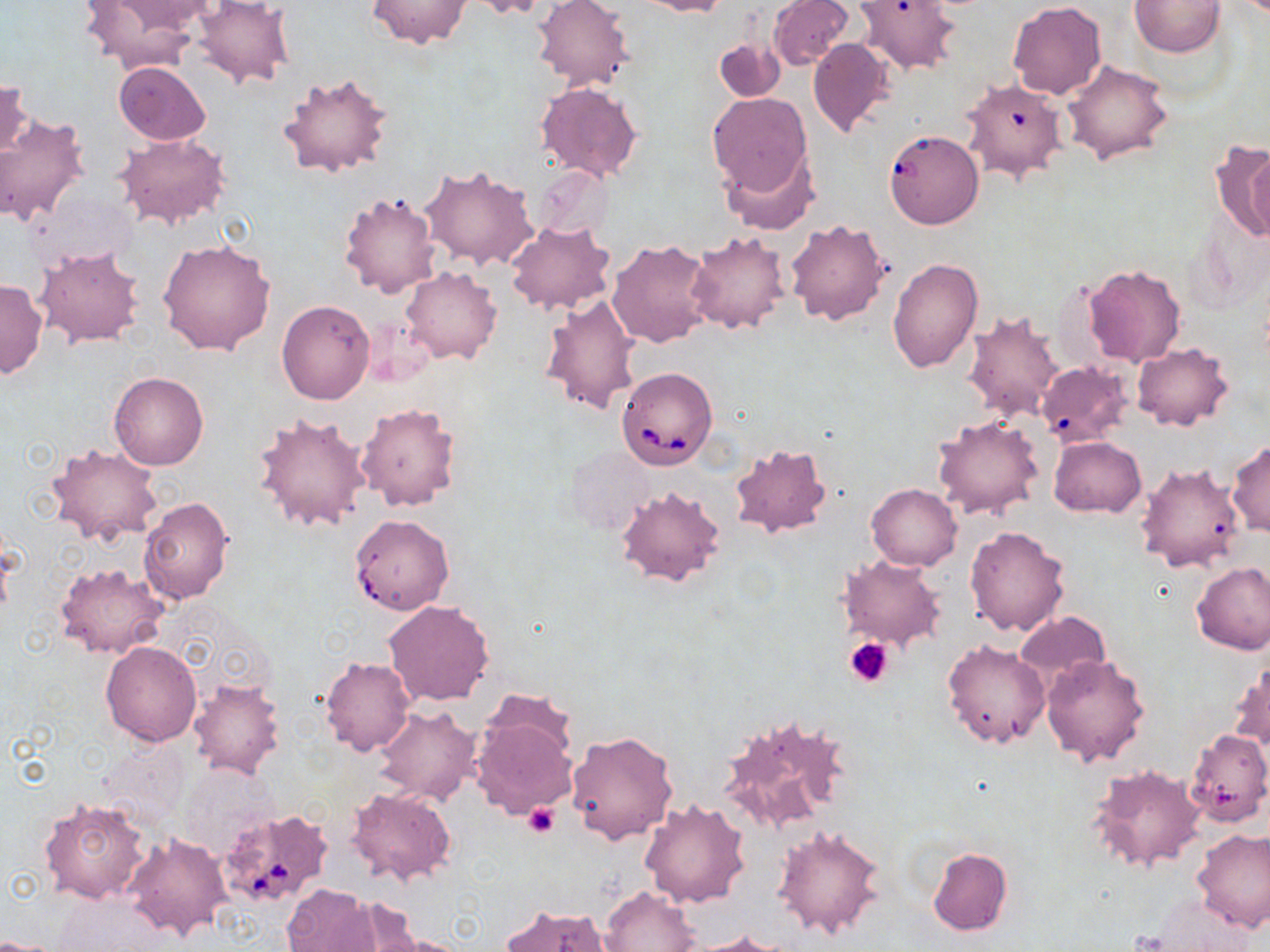 Approximate bounding boxes as (x1,y1)-(x2,y2) corner pairs in pixels. Platelet locations: (843,636)-(894,687), (524,802)-(559,839). Uninfected red blood cell locations: (365,0)-(474,49), (468,0)-(549,20), (531,0)-(633,91), (640,0)-(731,17), (767,0)-(853,71), (855,0)-(960,75), (1130,0)-(1225,57), (77,1)-(199,71), (105,1)-(217,36), (190,1)-(296,88), (1008,2)-(1107,99), (714,36)-(784,102), (807,38)-(895,138), (1063,60)-(1172,166), (112,62)-(212,145), (278,72)-(394,179), (1,76)-(33,168), (959,78)-(1067,185), (534,82)-(644,182), (707,93)-(812,195), (0,113)-(89,226), (887,130)-(986,234), (116,135)-(231,231), (1212,141)-(1270,240), (722,149)-(819,234), (420,165)-(538,272), (533,165)-(613,241), (339,192)-(441,299), (784,219)-(889,326), (506,220)-(616,314), (684,230)-(792,334), (156,238)-(276,355), (607,240)-(716,349), (33,244)-(146,349), (887,259)-(982,373), (1084,264)-(1186,366), (401,266)-(503,364), (0,279)-(46,378), (540,293)-(643,416), (277,300)-(376,405), (963,309)-(1065,422), (1131,341)-(1233,431), (1037,361)-(1133,445), (109,372)-(207,470), (356,401)-(461,510), (251,410)-(372,533), (932,416)-(1045,521), (1050,436)-(1146,516), (1228,441)-(1269,537), (45,442)-(164,548), (730,443)-(832,538), (565,446)-(654,538), (1136,461)-(1245,573), (616,484)-(727,587), (867,484)-(962,569), (138,495)-(234,604), (349,514)-(454,615), (965,525)-(1069,637), (838,556)-(947,652), (1191,560)-(1270,655), (56,562)-(169,660), (382,600)-(495,707), (1014,610)-(1110,693), (942,640)-(1049,749), (101,641)-(202,747), (1041,653)-(1150,767), (319,656)-(415,757), (1230,660)-(1270,756), (188,680)-(286,778), (372,704)-(480,806), (471,706)-(576,820), (718,710)-(855,837), (1185,729)-(1270,826), (566,731)-(679,845), (101,738)-(190,828), (182,764)-(280,860), (1088,764)-(1207,874), (346,786)-(459,887), (39,796)-(151,905), (638,798)-(750,907), (771,824)-(888,939), (1193,827)-(1270,932), (123,831)-(231,942), (927,848)-(1013,935), (282,884)-(381,952), (600,885)-(701,952), (1146,895)-(1256,950), (336,898)-(435,951), (499,903)-(611,951), (368,931)-(476,952), (688,931)-(792,952), (0,937)-(63,952). Babesia divergens-infected red blood cell locations: (615,367)-(717,469), (219,807)-(335,908). Slide-level diagnosis: Babesia divergens. May-Grünwald-Giemsa stain. Single field of view. Image is 1270×952 pixels. Light microscopy. Thin blood smear. 1000x magnification.